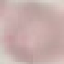

Summary:
  - Result: negative for malaria parasites
  - Stain: Giemsa
  - Image type: automatically extracted cell patch, resized to 64 × 64 pixels
  - Capture: smartphone camera at the microscope eyepiece
  - Preparation: thin blood film